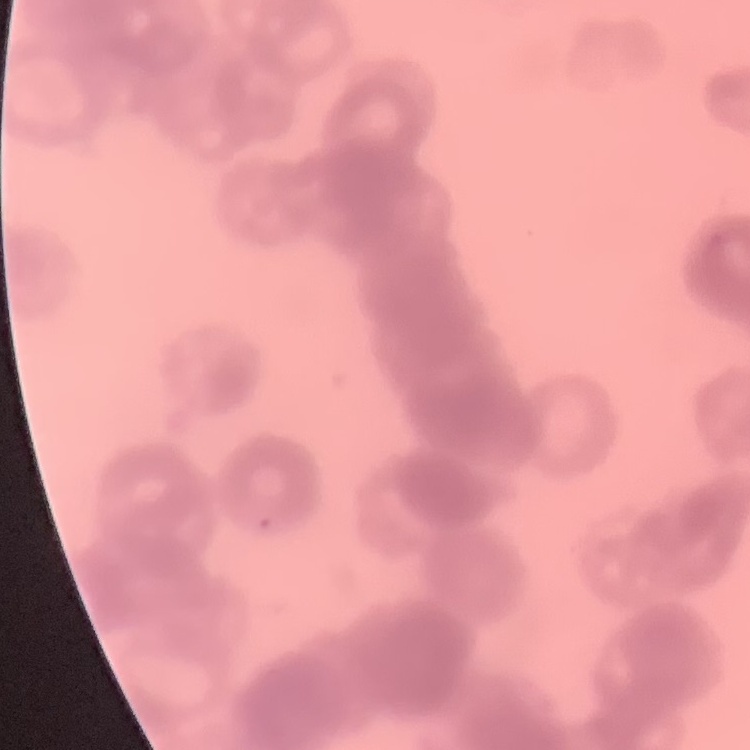 The red blood cells show rouleaux formation. Thin blood smear. One tile cut from a larger photomicrograph. Field's or Giemsa stain.